Locate every Plasmodium falciparum-infected red blood cell.
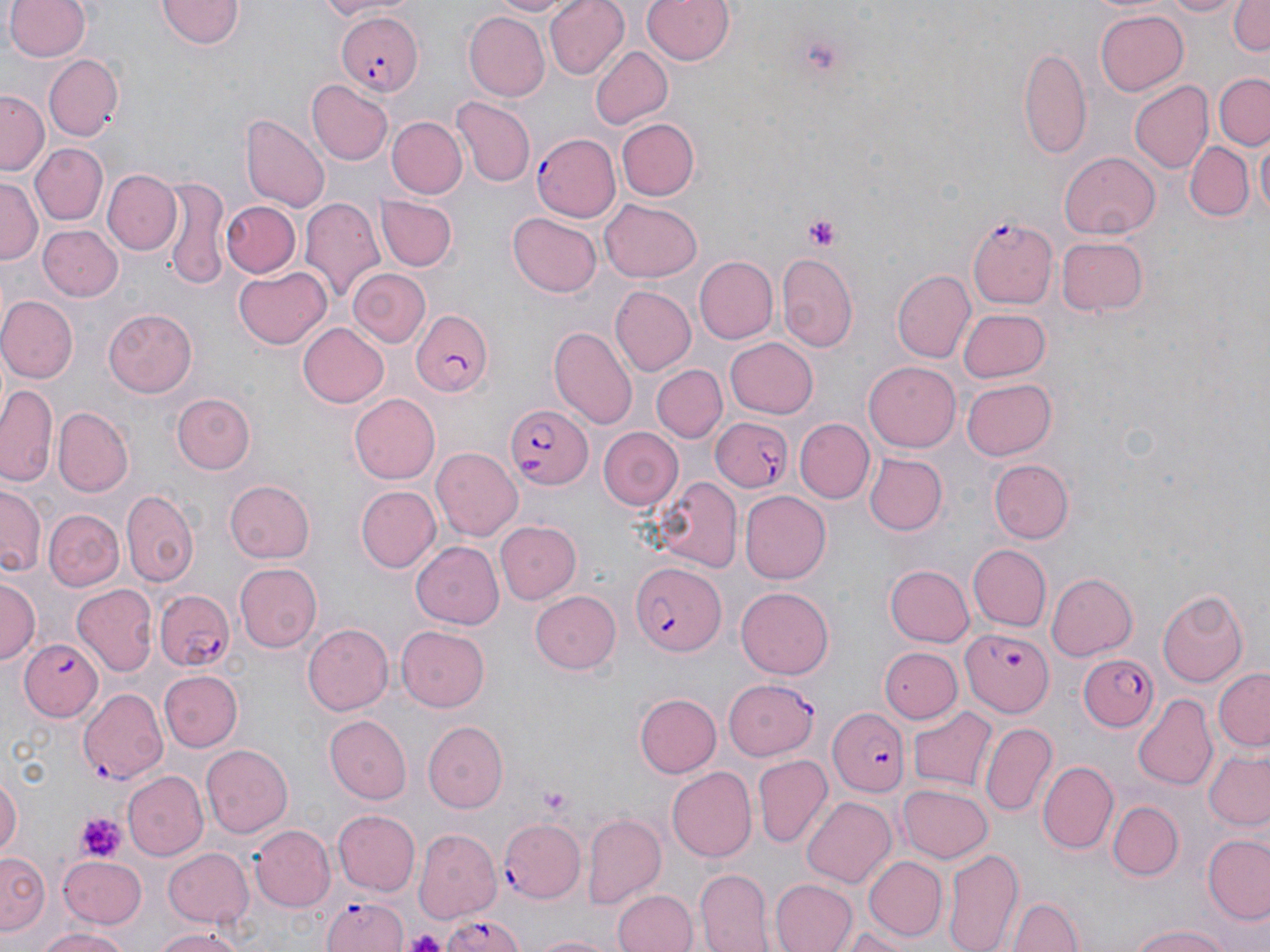

Approximate bounding boxes as [x1, y1, x2, y2] in pixels.
Plasmodium falciparum-infected red blood cells: [334, 10, 421, 94], [532, 133, 621, 223], [968, 217, 1058, 307], [408, 311, 495, 396], [505, 402, 595, 490], [709, 417, 795, 492], [630, 561, 724, 657], [152, 588, 234, 672], [964, 626, 1053, 716], [17, 639, 100, 722], [1077, 650, 1159, 733], [78, 688, 166, 784], [830, 708, 907, 795], [497, 820, 585, 904], [319, 894, 409, 950], [436, 910, 530, 952].

slide_level_diagnosis: Plasmodium falciparum
stain: May-Grünwald-Giemsa
modality: optical microscopy
preparation: thin blood smear
platelet_locations: 'approximate bounding boxes as [x1, y1, x2, y2] in pixels: [802, 214, 841, 249], [537, 787, 572, 813], [78, 813, 125, 862], [404, 931, 446, 952]'
magnification: 1000x
field_of_view: single
uninfected_red_blood_cell_locations: 'approximate bounding boxes as [x1, y1, x2, y2] in pixels: [309, 0, 405, 21], [485, 0, 583, 18], [543, 0, 628, 80], [641, 0, 735, 66], [1153, 0, 1245, 18], [1231, 0, 1270, 57], [5, 1, 92, 63], [158, 1, 242, 51], [1094, 10, 1189, 96], [465, 11, 550, 101], [1021, 46, 1093, 162], [589, 47, 671, 130], [44, 55, 124, 140], [1212, 73, 1270, 149], [308, 79, 393, 164], [1128, 81, 1211, 173], [0, 90, 48, 172], [452, 97, 536, 187], [242, 114, 331, 210], [387, 117, 467, 199], [616, 118, 699, 201], [1255, 131, 1269, 218], [1184, 140, 1251, 222], [31, 143, 108, 224], [1060, 150, 1160, 239], [104, 169, 179, 255], [159, 176, 229, 290], [0, 179, 42, 265], [369, 187, 451, 332], [376, 197, 457, 270], [300, 199, 385, 306], [600, 199, 705, 283], [221, 201, 300, 277], [508, 212, 602, 298], [40, 223, 121, 301], [1057, 234, 1149, 317], [776, 252, 859, 352], [694, 256, 778, 344], [233, 266, 330, 350], [349, 267, 429, 346], [894, 271, 975, 362], [613, 286, 696, 375], [0, 295, 77, 382], [957, 305, 1051, 382], [104, 309, 198, 398], [296, 322, 389, 408], [550, 327, 637, 431], [724, 337, 817, 419], [865, 360, 962, 449], [651, 364, 727, 443], [962, 378, 1057, 459], [2, 383, 60, 487], [803, 391, 907, 495], [174, 392, 256, 474], [349, 393, 439, 483], [54, 407, 132, 494], [794, 418, 874, 503], [599, 426, 683, 510], [433, 448, 521, 540], [866, 453, 947, 534], [989, 460, 1073, 543], [650, 476, 744, 570], [226, 480, 315, 563], [358, 485, 440, 572], [1, 487, 42, 576], [122, 489, 197, 586], [739, 489, 830, 580], [45, 508, 124, 591], [496, 519, 580, 603], [411, 541, 502, 629], [967, 542, 1050, 630], [881, 553, 1049, 638], [234, 562, 323, 653], [885, 563, 974, 646], [1045, 573, 1136, 661], [1, 576, 41, 662], [74, 585, 157, 677], [737, 586, 834, 680], [1157, 589, 1250, 687], [531, 590, 621, 675], [303, 622, 393, 715], [395, 627, 491, 713], [881, 645, 962, 724], [1213, 668, 1269, 752], [158, 670, 242, 753], [724, 678, 818, 759], [635, 694, 720, 778], [1134, 695, 1217, 789], [909, 707, 996, 793], [324, 715, 411, 804], [424, 719, 509, 812], [981, 720, 1058, 816], [201, 744, 293, 837], [1202, 749, 1270, 830], [752, 755, 832, 848], [1038, 760, 1117, 853], [667, 767, 756, 862], [0, 771, 21, 865], [123, 772, 208, 861], [898, 783, 993, 863], [801, 794, 896, 885], [1109, 800, 1182, 881], [332, 809, 421, 896], [581, 812, 667, 906], [248, 823, 337, 913], [412, 832, 499, 927], [1204, 835, 1270, 925], [942, 845, 1025, 952], [163, 846, 255, 929], [1, 850, 51, 938], [57, 855, 147, 928], [864, 855, 945, 940], [696, 868, 772, 952], [770, 878, 858, 952], [614, 889, 695, 952], [1010, 893, 1082, 952], [1124, 921, 1234, 952], [150, 926, 249, 952], [839, 926, 917, 951], [34, 929, 133, 952], [523, 932, 619, 952]'
image_size: 1270×952 pixels